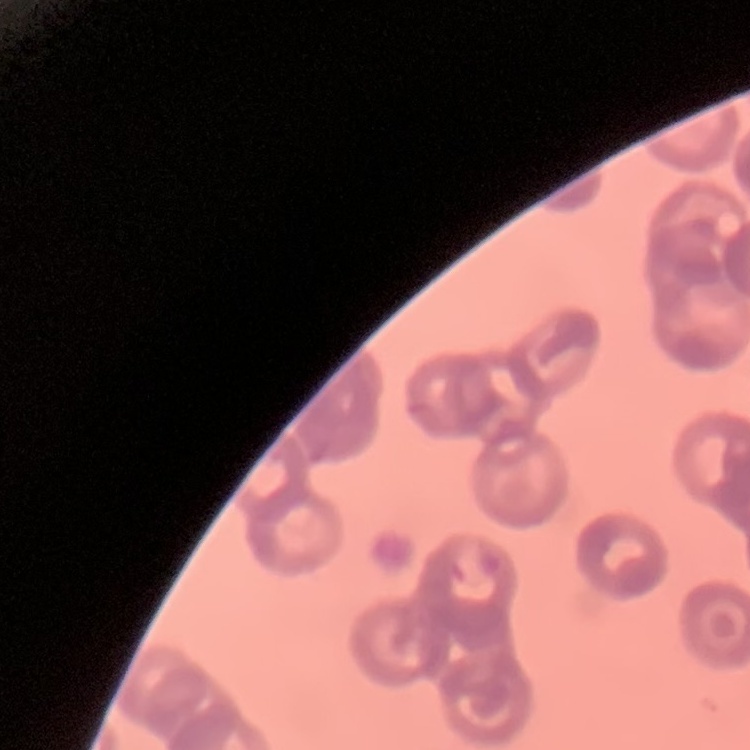
red blood cell morphology = rouleaux formation
image type = square crop of a larger photomicrograph
stain = Field's or Giemsa
preparation = thin blood film